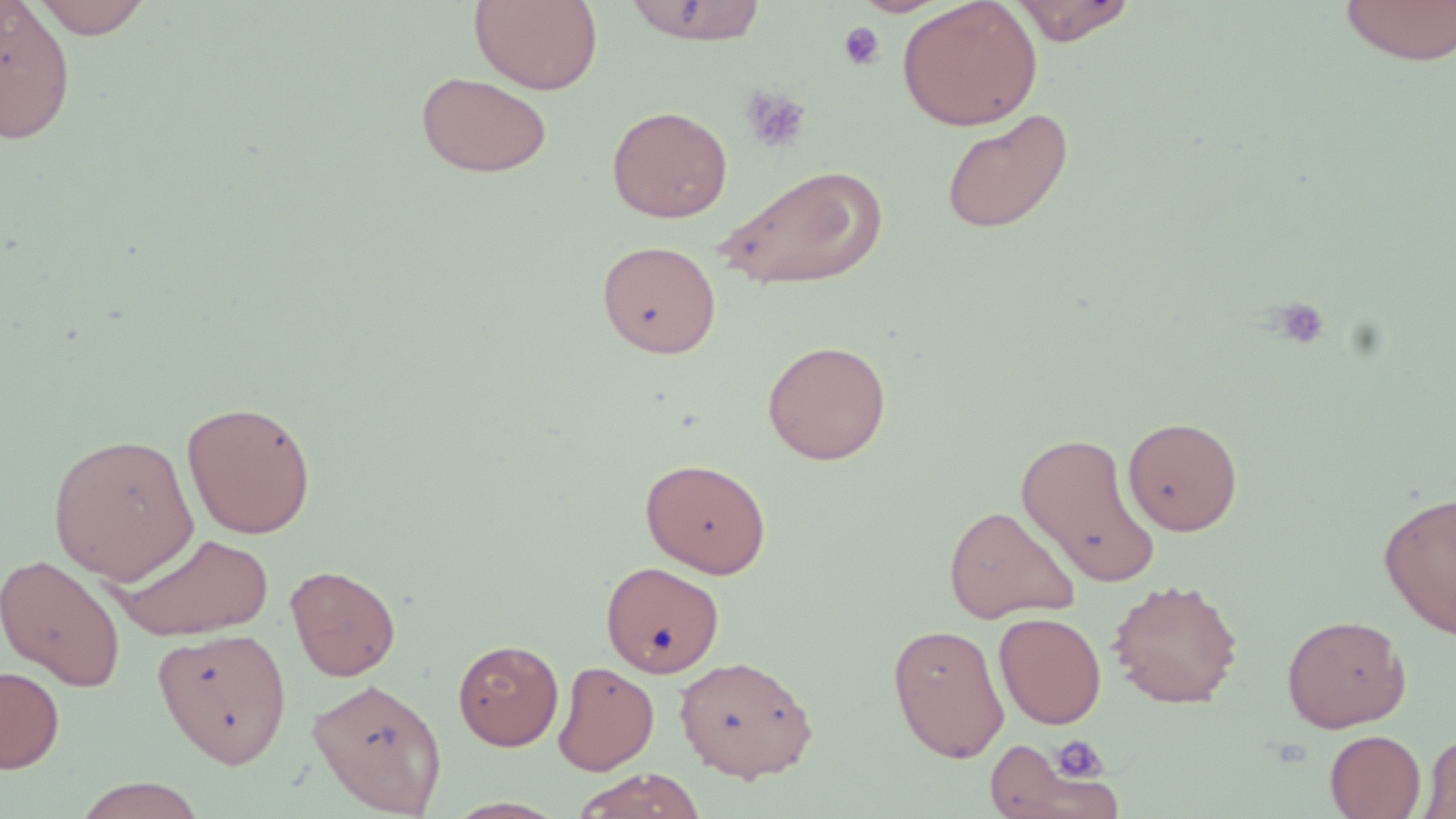

{
  "slide_level_diagnosis": "no evidence of blood parasites",
  "field_of_view": "one of a larger specimen",
  "platelet_locations": "approximate bounding boxes as [x1, y1, x2, y2] in pixels: [838, 20, 886, 72], [739, 86, 811, 154], [1271, 298, 1331, 351], [1050, 736, 1108, 780]",
  "modality": "light microscopy",
  "stain": "May-Grünwald-Giemsa",
  "magnification": "1000x",
  "preparation": "thin blood smear",
  "uninfected_red_blood_cell_locations": "approximate bounding boxes as [x1, y1, x2, y2] in pixels: [30, 0, 153, 38], [469, 0, 603, 94], [624, 0, 768, 45], [897, 0, 1042, 131], [1008, 0, 1139, 45], [1338, 0, 1456, 66], [1, 1, 76, 145], [415, 71, 553, 179], [607, 105, 732, 222], [941, 108, 1074, 234], [716, 164, 888, 290], [596, 239, 721, 358], [762, 339, 892, 465], [181, 400, 317, 539], [1123, 416, 1243, 536], [1015, 431, 1162, 589], [46, 432, 199, 584], [640, 458, 772, 578], [1378, 489, 1456, 641], [943, 504, 1079, 623], [108, 532, 276, 641], [0, 554, 126, 693], [598, 561, 728, 682], [285, 564, 401, 681], [1107, 578, 1244, 709], [994, 612, 1107, 729], [1282, 614, 1411, 732], [887, 623, 1010, 762], [154, 626, 292, 767], [453, 639, 563, 750], [674, 654, 818, 782], [553, 660, 659, 775], [0, 665, 65, 774], [307, 677, 447, 816], [1325, 730, 1426, 818], [1419, 731, 1456, 819], [983, 735, 1123, 819], [571, 768, 707, 819], [71, 777, 209, 818]",
  "image_size": "1456×819 pixels"
}